Locate and identify every blood parasite.
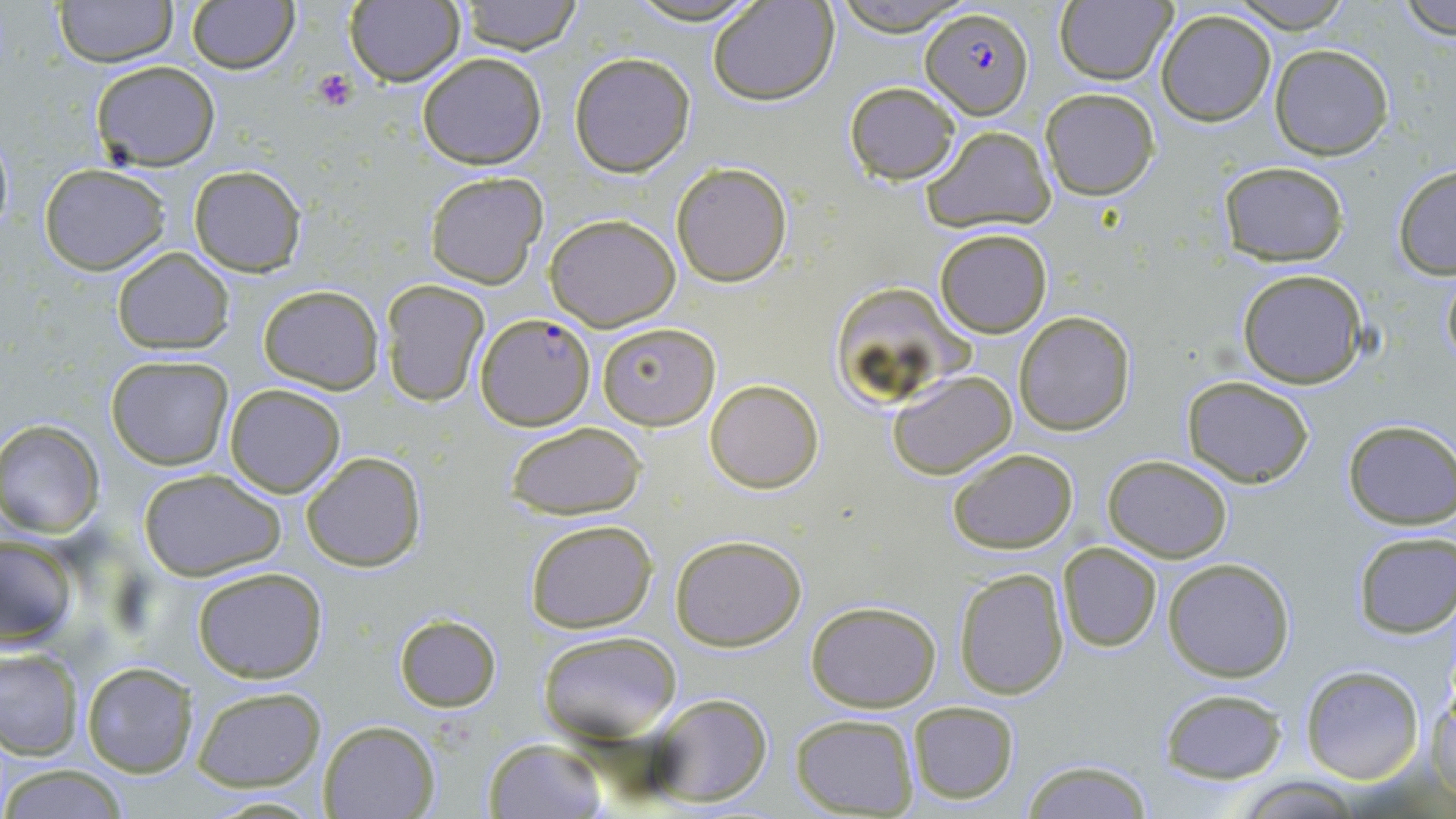
Approximate bounding boxes as (x1, y1, x2, y2) in pixels.
Plasmodium falciparum-infected red blood cells: (921, 7, 1032, 119), (475, 313, 595, 429).
No Plasmodium ovale, Plasmodium malariae, Plasmodium vivax, Babesia divergens, or Trypanosoma brucei observed.

Platelet locations: (310, 69, 357, 111). Uninfected red blood cell locations: (52, 0, 177, 67), (346, 0, 465, 88), (457, 0, 582, 55), (625, 0, 765, 25), (830, 0, 970, 36), (1228, 0, 1358, 31), (186, 1, 299, 74), (708, 1, 839, 105), (1398, 1, 1456, 37), (1054, 2, 1175, 84), (1155, 8, 1277, 126), (1270, 44, 1393, 160), (418, 53, 547, 169), (569, 54, 694, 176), (90, 60, 220, 170), (843, 81, 961, 183), (1040, 88, 1159, 200), (921, 125, 1057, 232), (671, 160, 794, 286), (1216, 160, 1350, 264), (39, 165, 170, 275), (1391, 165, 1456, 280), (187, 166, 306, 276), (425, 170, 548, 288), (545, 213, 681, 331), (933, 227, 1052, 337), (112, 247, 234, 353), (1439, 265, 1456, 372), (1236, 270, 1368, 388), (380, 280, 489, 406), (830, 283, 979, 404), (258, 285, 383, 392), (1014, 311, 1136, 435), (597, 321, 720, 430), (105, 354, 234, 469), (887, 369, 1016, 479), (1182, 377, 1315, 487), (705, 380, 823, 493), (224, 384, 346, 497), (1341, 420, 1455, 529), (503, 421, 646, 519), (0, 422, 103, 536), (946, 447, 1078, 553), (302, 452, 424, 572), (1103, 455, 1232, 562), (138, 467, 287, 581), (526, 519, 657, 632), (1351, 530, 1455, 639), (1, 534, 82, 650), (669, 534, 808, 651), (1058, 542, 1162, 652), (1163, 558, 1295, 681), (191, 566, 328, 683), (952, 567, 1070, 699), (806, 601, 941, 713), (394, 615, 501, 712), (537, 630, 682, 745), (0, 648, 83, 759), (80, 660, 198, 779), (1300, 666, 1424, 784), (1429, 678, 1456, 798), (191, 685, 327, 791), (1158, 688, 1287, 784), (648, 692, 774, 807), (907, 701, 1020, 805), (791, 713, 919, 817), (319, 719, 438, 818), (481, 738, 608, 819), (1019, 760, 1156, 817), (3, 766, 131, 818), (1236, 777, 1364, 817). Slide-level diagnosis: Plasmodium falciparum. Light microscopy. 1000x magnification. One field of a larger specimen. May-Grünwald-Giemsa-stained preparation. Image is 1456×819 pixels. Thin blood smear.